State the blood parasite species.
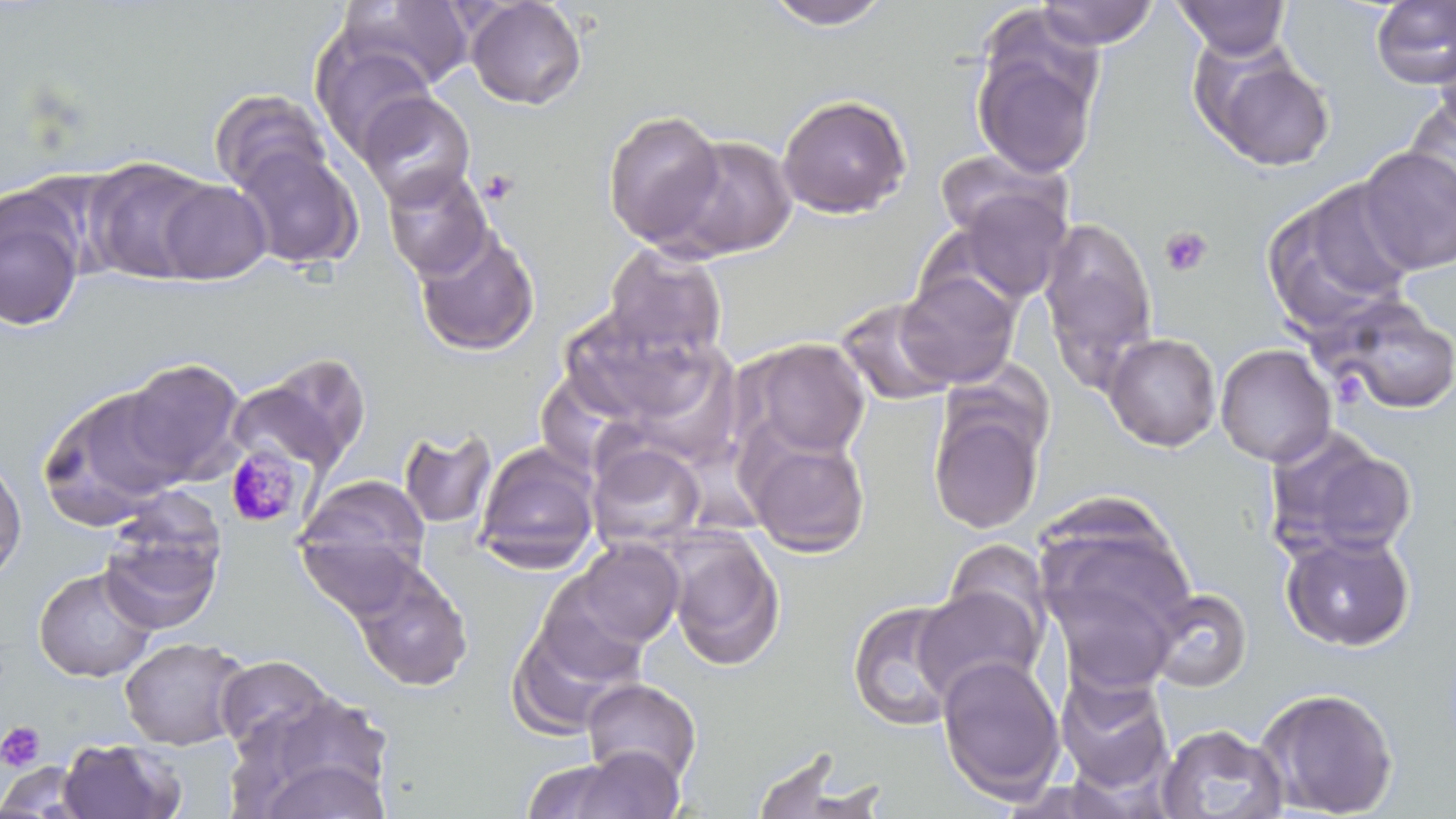

Plasmodium malariae.

Summary:
  - Coordinate format: approximate bounding boxes as named x1/y1/x2/y2 corners in pixels
  - Platelet locations: (x1=478, y1=168, x2=521, y2=205), (x1=1159, y1=225, x2=1213, y2=277), (x1=1331, y1=370, x2=1368, y2=407), (x1=0, y1=721, x2=46, y2=772)
  - Uninfected red blood cell locations: (x1=338, y1=0, x2=473, y2=91), (x1=465, y1=0, x2=587, y2=110), (x1=1173, y1=0, x2=1291, y2=59), (x1=1371, y1=0, x2=1456, y2=90), (x1=760, y1=1, x2=893, y2=29), (x1=1035, y1=1, x2=1160, y2=49), (x1=311, y1=37, x2=437, y2=158), (x1=1432, y1=37, x2=1456, y2=144), (x1=972, y1=39, x2=1101, y2=179), (x1=1198, y1=48, x2=1336, y2=172), (x1=209, y1=88, x2=329, y2=196), (x1=356, y1=90, x2=476, y2=210), (x1=777, y1=93, x2=912, y2=218), (x1=1404, y1=96, x2=1456, y2=216), (x1=602, y1=109, x2=727, y2=249), (x1=664, y1=134, x2=798, y2=260), (x1=232, y1=144, x2=363, y2=271), (x1=1356, y1=146, x2=1456, y2=275), (x1=934, y1=148, x2=1069, y2=244), (x1=84, y1=157, x2=222, y2=285), (x1=381, y1=166, x2=493, y2=280), (x1=1260, y1=178, x2=1420, y2=337), (x1=154, y1=180, x2=272, y2=284), (x1=953, y1=187, x2=1072, y2=303), (x1=0, y1=189, x2=86, y2=333), (x1=1038, y1=217, x2=1159, y2=389), (x1=412, y1=225, x2=540, y2=357), (x1=601, y1=243, x2=728, y2=362), (x1=896, y1=268, x2=1021, y2=389), (x1=1316, y1=296, x2=1456, y2=415), (x1=835, y1=297, x2=959, y2=406), (x1=562, y1=315, x2=718, y2=427), (x1=1104, y1=332, x2=1221, y2=451), (x1=742, y1=337, x2=871, y2=459), (x1=1215, y1=343, x2=1336, y2=467), (x1=653, y1=345, x2=741, y2=455), (x1=230, y1=352, x2=373, y2=480), (x1=119, y1=357, x2=248, y2=485), (x1=938, y1=357, x2=1055, y2=447), (x1=532, y1=364, x2=646, y2=462), (x1=36, y1=383, x2=189, y2=529), (x1=928, y1=405, x2=1046, y2=535), (x1=398, y1=426, x2=498, y2=530), (x1=740, y1=429, x2=872, y2=558), (x1=1268, y1=429, x2=1418, y2=561), (x1=473, y1=440, x2=601, y2=574), (x1=587, y1=440, x2=707, y2=550), (x1=0, y1=451, x2=27, y2=583), (x1=296, y1=475, x2=432, y2=589), (x1=1034, y1=504, x2=1196, y2=658), (x1=98, y1=511, x2=225, y2=637), (x1=665, y1=531, x2=786, y2=670), (x1=1279, y1=531, x2=1416, y2=652), (x1=296, y1=534, x2=421, y2=623), (x1=943, y1=538, x2=1055, y2=646), (x1=569, y1=539, x2=685, y2=649), (x1=347, y1=558, x2=473, y2=692), (x1=33, y1=566, x2=158, y2=683), (x1=533, y1=576, x2=652, y2=688), (x1=912, y1=586, x2=1044, y2=702), (x1=1146, y1=587, x2=1253, y2=692), (x1=846, y1=599, x2=966, y2=732), (x1=507, y1=620, x2=635, y2=738), (x1=119, y1=636, x2=249, y2=751), (x1=215, y1=654, x2=334, y2=753), (x1=936, y1=655, x2=1066, y2=803), (x1=1055, y1=671, x2=1174, y2=794), (x1=581, y1=677, x2=702, y2=787), (x1=1255, y1=686, x2=1400, y2=818), (x1=237, y1=698, x2=394, y2=816), (x1=1156, y1=723, x2=1288, y2=819), (x1=56, y1=739, x2=184, y2=819), (x1=548, y1=747, x2=686, y2=819), (x1=747, y1=751, x2=882, y2=819), (x1=254, y1=758, x2=392, y2=818), (x1=0, y1=762, x2=93, y2=818)
  - Plasmodium malariae-infected red blood cell locations: (x1=224, y1=445, x2=304, y2=528)
  - Stain: May-Grünwald-Giemsa
  - Image size: 1456×819 pixels
  - Field of view: one of a larger specimen
  - Magnification: 1000x
  - Preparation: thin blood smear
  - Modality: light microscopy